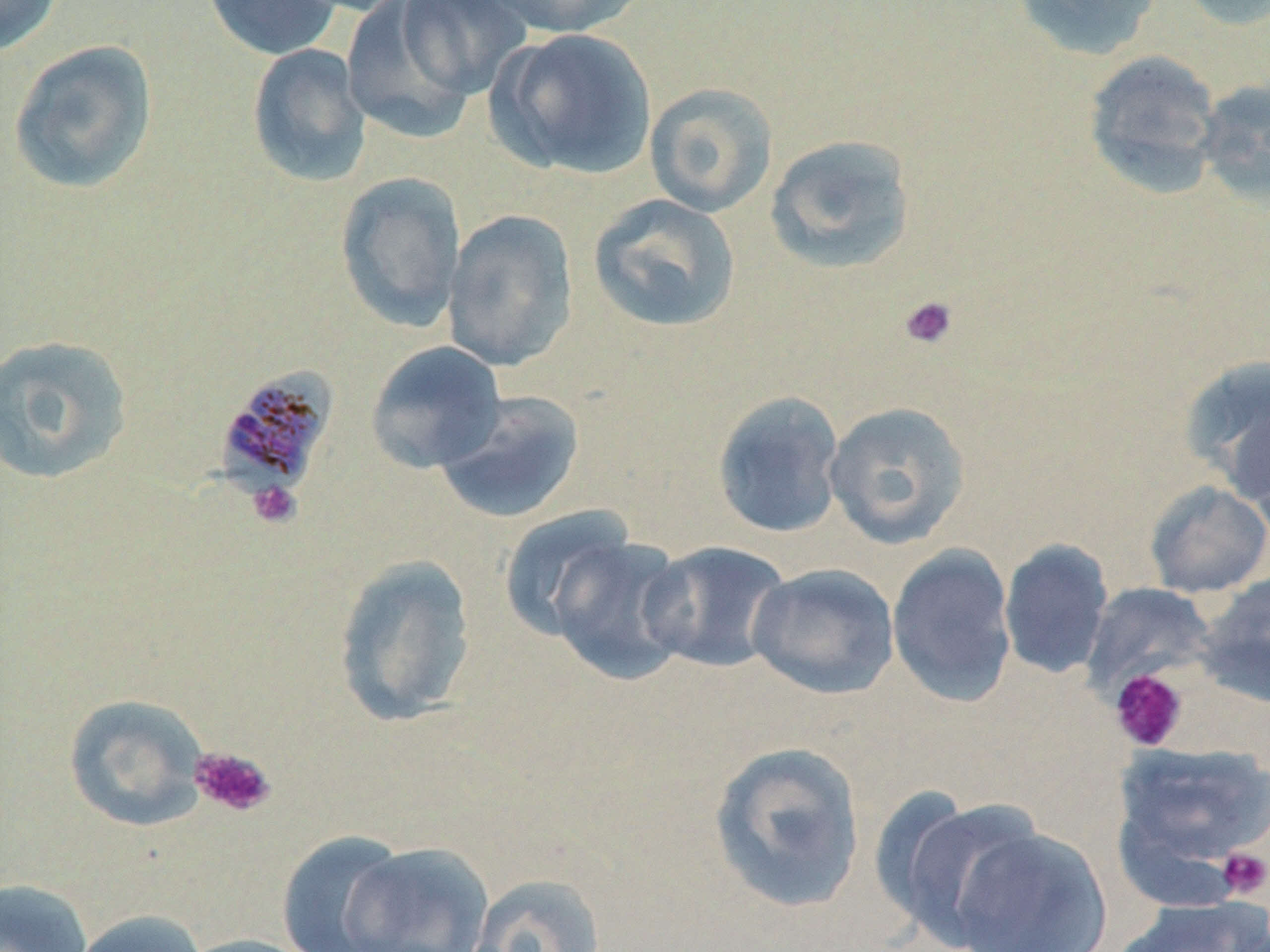
Plasmodium malariae-infected red blood cell locations = approximate bounding boxes as named x1/y1/x2/y2 corners in pixels: (x1=213, y1=366, x2=338, y2=501)
slide-level diagnosis = Plasmodium malariae
preparation = thin blood smear
uninfected red blood cell locations = approximate bounding boxes as named x1/y1/x2/y2 corners in pixels: (x1=0, y1=0, x2=65, y2=57), (x1=201, y1=0, x2=342, y2=60), (x1=394, y1=0, x2=533, y2=103), (x1=482, y1=0, x2=646, y2=39), (x1=1011, y1=0, x2=1166, y2=61), (x1=1176, y1=0, x2=1270, y2=31), (x1=342, y1=2, x2=484, y2=142), (x1=489, y1=26, x2=659, y2=181), (x1=8, y1=39, x2=159, y2=196), (x1=246, y1=43, x2=371, y2=187), (x1=1083, y1=50, x2=1224, y2=197), (x1=1194, y1=77, x2=1270, y2=208), (x1=644, y1=82, x2=779, y2=217), (x1=764, y1=133, x2=917, y2=275), (x1=335, y1=170, x2=467, y2=332), (x1=587, y1=193, x2=742, y2=334), (x1=442, y1=209, x2=579, y2=372), (x1=0, y1=334, x2=135, y2=487), (x1=365, y1=340, x2=506, y2=474), (x1=1179, y1=355, x2=1270, y2=502), (x1=711, y1=389, x2=845, y2=539), (x1=434, y1=390, x2=586, y2=525), (x1=823, y1=401, x2=972, y2=549), (x1=1144, y1=479, x2=1270, y2=598), (x1=498, y1=506, x2=639, y2=643), (x1=542, y1=532, x2=694, y2=685), (x1=999, y1=538, x2=1114, y2=679), (x1=641, y1=540, x2=792, y2=674), (x1=887, y1=544, x2=1018, y2=707), (x1=331, y1=554, x2=478, y2=728), (x1=747, y1=563, x2=899, y2=700), (x1=1195, y1=571, x2=1270, y2=707), (x1=1081, y1=583, x2=1217, y2=696), (x1=62, y1=693, x2=211, y2=832), (x1=1110, y1=739, x2=1270, y2=893), (x1=707, y1=740, x2=867, y2=914), (x1=877, y1=792, x2=1047, y2=949), (x1=946, y1=824, x2=1115, y2=952), (x1=275, y1=831, x2=412, y2=952), (x1=341, y1=840, x2=494, y2=952), (x1=463, y1=872, x2=609, y2=952), (x1=0, y1=877, x2=94, y2=952), (x1=1112, y1=897, x2=1270, y2=952), (x1=70, y1=908, x2=208, y2=952), (x1=175, y1=934, x2=321, y2=952)
modality = light microscopy
stain = May-Grünwald-Giemsa
platelet locations = approximate bounding boxes as named x1/y1/x2/y2 corners in pixels: (x1=898, y1=295, x2=959, y2=351), (x1=247, y1=480, x2=302, y2=530), (x1=1109, y1=669, x2=1189, y2=752), (x1=189, y1=746, x2=277, y2=818), (x1=1216, y1=847, x2=1270, y2=900)
field of view = single
magnification = 1000x
image size = 1270×952 pixels